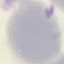

result = no malaria parasites seen
capture = smartphone through the microscope eyepiece
image type = automatically extracted cell patch, resized to 64 × 64 pixels
stain = Giemsa
preparation = thin smear